Report the malaria status of this cell.
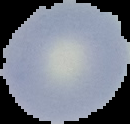

Uninfected.

From a thin blood film. Cell region segmented out of the field of view; the surrounding area is masked to black. Image is 130×124 pixels.